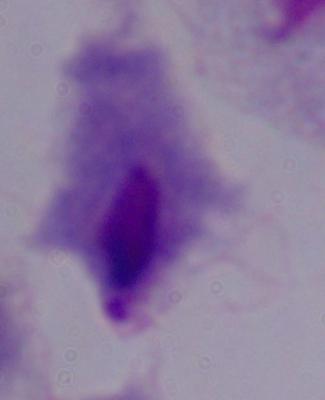
Summary:
  - Modality: micrograph
  - Magnification: 1000x
  - Identification: trichomonad